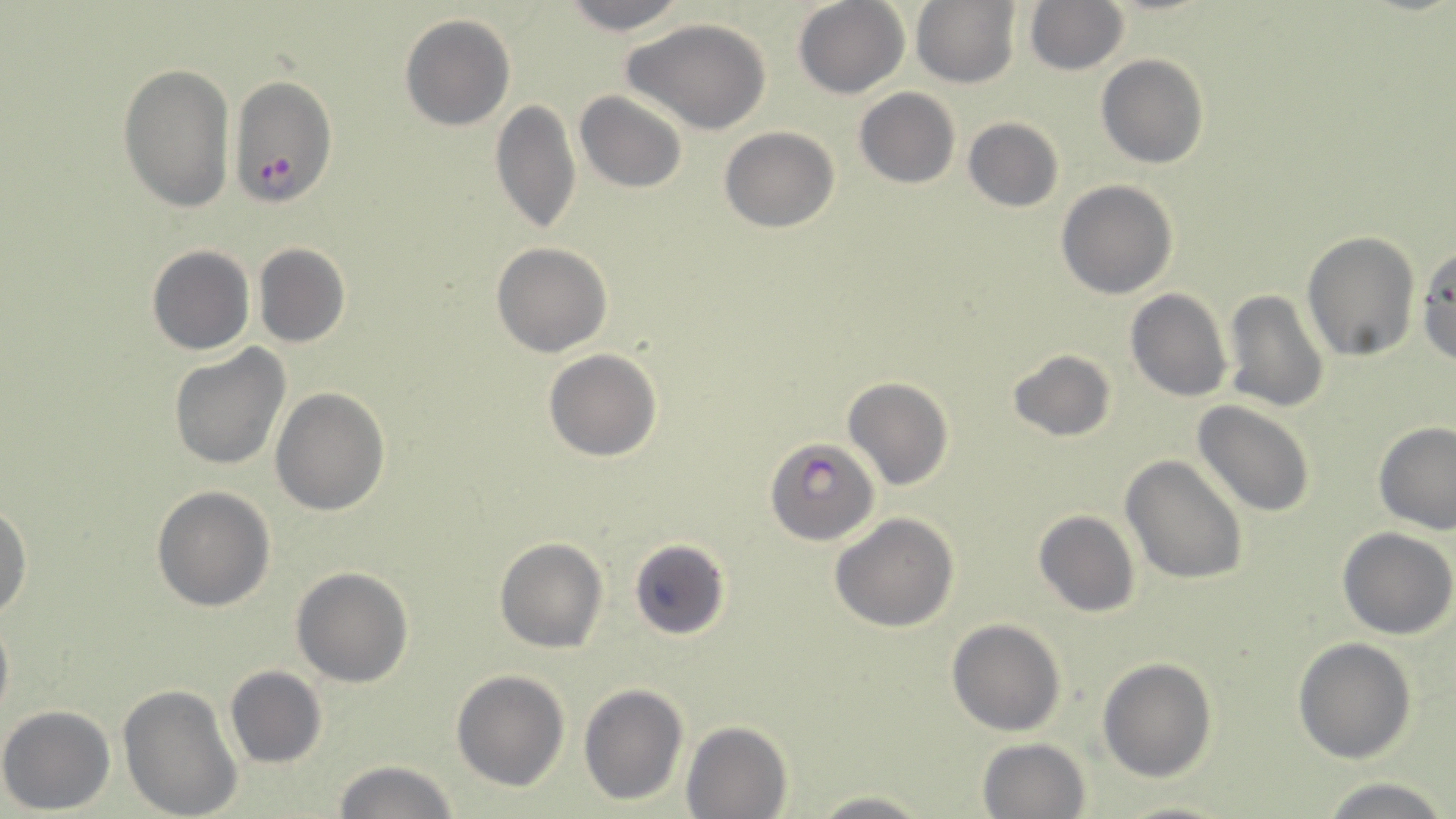
slide-level diagnosis = Plasmodium falciparum
magnification = 1000x
Plasmodium falciparum-infected red blood cell locations = approximate bounding boxes as (x1, y1, x2, y2) in pixels: (228, 75, 339, 206), (767, 438, 878, 547)
field of view = one of a larger specimen
preparation = thin blood smear
modality = light microscopy
uninfected red blood cell locations = approximate bounding boxes as (x1, y1, x2, y2) in pixels: (559, 0, 693, 35), (793, 0, 908, 98), (911, 1, 1021, 87), (1023, 1, 1129, 76), (399, 14, 516, 132), (626, 19, 773, 134), (1096, 54, 1209, 169), (118, 62, 236, 214), (854, 88, 960, 188), (575, 92, 687, 192), (490, 100, 581, 238), (960, 116, 1063, 214), (720, 126, 841, 233), (488, 134, 590, 322), (1055, 179, 1178, 299), (1301, 231, 1420, 361), (491, 241, 612, 356), (253, 243, 350, 348), (146, 245, 254, 355), (1416, 246, 1456, 367), (1125, 288, 1232, 402), (1221, 289, 1330, 414), (168, 344, 292, 470), (543, 348, 661, 461), (1006, 349, 1117, 442), (842, 378, 954, 491), (271, 386, 390, 515), (1191, 400, 1318, 518), (1374, 421, 1455, 533), (1120, 455, 1249, 584), (151, 485, 275, 612), (0, 504, 32, 622), (1032, 509, 1141, 618), (830, 512, 960, 633), (1337, 527, 1455, 640), (495, 538, 608, 654), (627, 538, 731, 640), (291, 566, 414, 688), (0, 605, 13, 731), (946, 618, 1067, 737), (1293, 637, 1418, 763), (1098, 656, 1217, 782), (225, 665, 327, 768), (450, 670, 570, 791), (578, 682, 688, 806), (117, 683, 244, 819), (0, 705, 115, 814), (681, 720, 793, 819), (977, 737, 1091, 819), (332, 760, 461, 817), (1319, 775, 1451, 819), (807, 791, 934, 819), (1114, 796, 1240, 819)
stain = May-Grünwald-Giemsa
image size = 1456×819 pixels